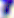

Captured at 400x magnification. Toxoplasma gondii is seen. Photomicrograph.